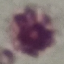

Summary:
  - Malaria status: uninfected
  - Capture: smartphone camera at the microscope eyepiece
  - Image type: automatically extracted cell patch, resized to 64 × 64 pixels
  - Preparation: thin smear
  - Stain: Giemsa